Report the malaria status of this cell.
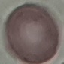

It is uninfected.

Cell patch, automatically extracted from a larger field of view and resized to 64 × 64 pixels. Acquired by smartphone through the microscope eyepiece. Giemsa stain. Thin blood film.